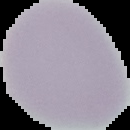
Summary:
  - Result: no malaria parasites seen
  - Image type: cell region segmented out of the field of view; surrounding area masked to black
  - Preparation: thin blood smear
  - Image size: 130×130 pixels